Identify the blood parasite species.
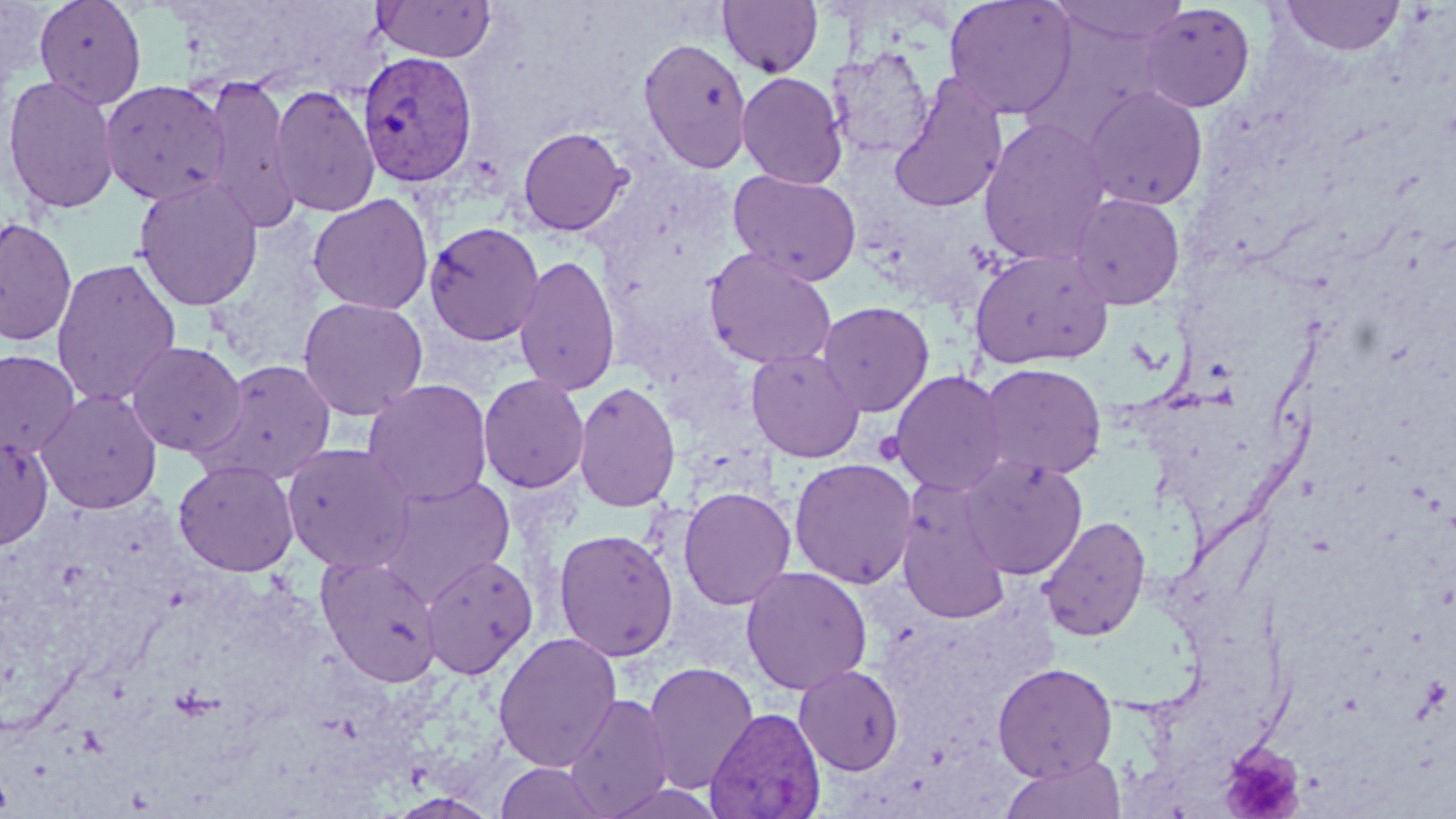
Plasmodium vivax.

field of view = single
Plasmodium vivax-infected red blood cell locations = approximate bounding boxes as (x1,y1)-(x2,y2) corner pairs in pixels: (357,51)-(478,187), (705,707)-(826,819)
platelet locations (subset) = approximate bounding boxes as (x1,y1)-(x2,y2) corner pairs in pixels: (871,430)-(907,466)
uninfected red blood cell locations (subset) = approximate bounding boxes as (x1,y1)-(x2,y2) corner pairs in pixels: (33,0)-(147,108), (372,0)-(497,62), (718,0)-(823,78), (944,0)-(1078,120), (1046,0)-(1191,49), (1278,0)-(1405,56), (1139,3)-(1256,113), (638,37)-(753,173), (827,47)-(934,160), (737,71)-(848,189), (2,74)-(120,214), (889,75)-(1009,215), (200,76)-(301,234), (99,79)-(230,206), (270,84)-(380,219), (1081,86)-(1208,211), (978,117)-(1112,266), (517,126)-(631,236), (728,169)-(862,286), (132,177)-(263,311), (1067,192)-(1185,310), (307,193)-(434,315), (0,216)-(77,346), (423,221)-(545,347), (703,248)-(838,370), (970,248)-(1114,369), (513,253)-(621,396), (51,258)-(182,408), (297,296)-(429,420), (817,301)-(935,417), (126,340)-(247,457), (745,347)-(866,463), (0,349)-(80,458), (195,359)-(338,485), (978,363)-(1107,480), (889,370)-(1010,497), (477,373)-(590,493), (363,379)-(493,505), (573,381)-(682,513), (35,388)-(163,515), (0,431)-(55,551), (282,442)-(416,574), (961,456)-(1088,579), (789,457)-(918,589), (173,459)-(300,577), (379,474)-(517,600), (895,481)-(1013,625), (678,486)-(797,610), (1038,515)-(1151,642), (553,528)-(678,661), (315,553)-(442,687), (420,553)-(538,680), (740,565)-(873,695), (493,632)-(623,772), (642,661)-(760,795), (992,662)-(1118,781), (794,664)-(904,775), (563,692)-(674,817), (998,755)-(1128,819), (494,761)-(612,819), (599,780)-(728,819), (386,793)-(502,818)
image size = 1456×819 pixels
modality = optical microscopy
stain = May-Grünwald-Giemsa
preparation = thin blood smear
magnification = 1000x